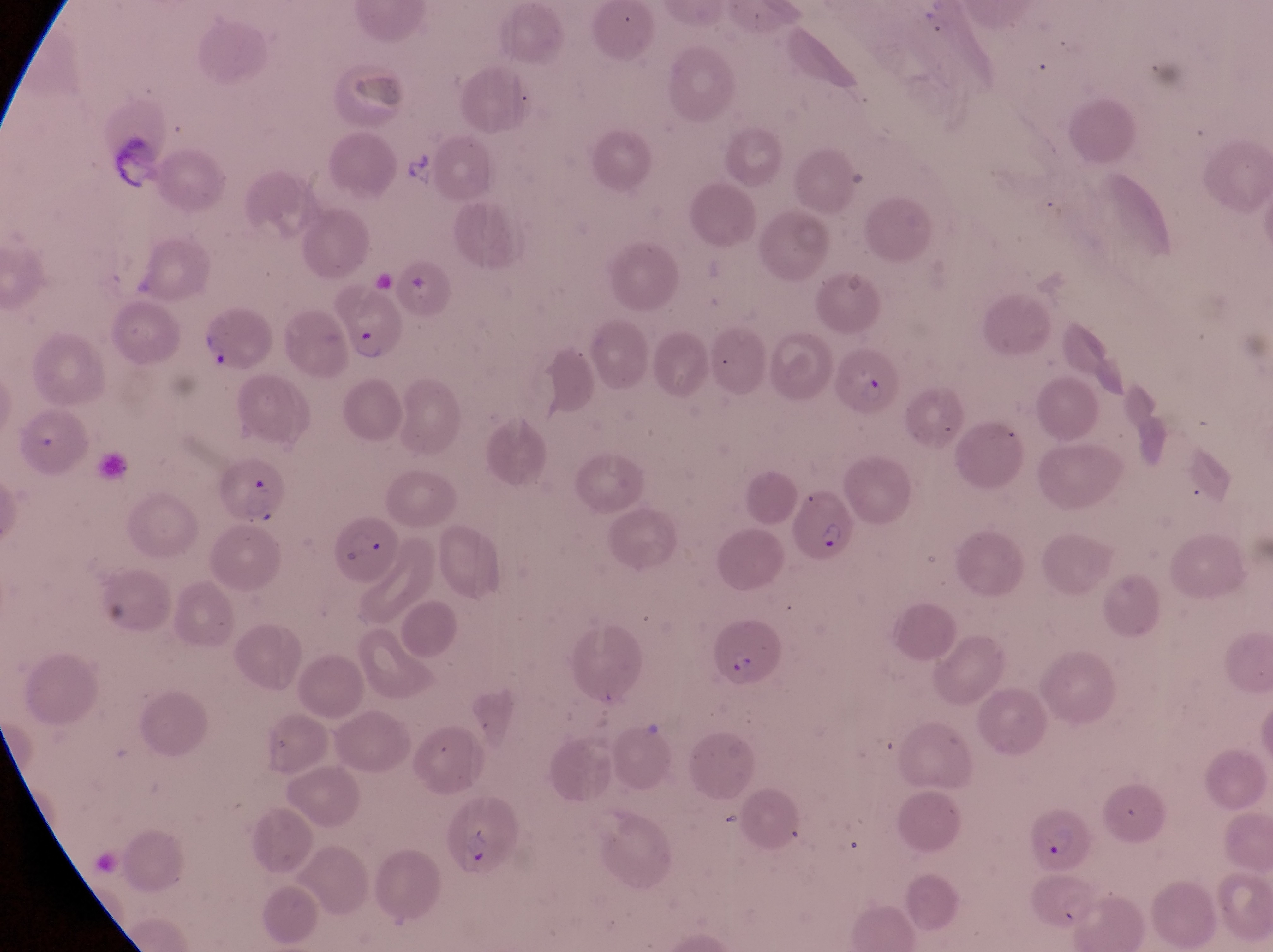

Approximate bounding boxes as {left, top, right, bottom} in pixels.
Summary:
  - Parasitised red blood cell locations: {339, 290, 402, 364}, {836, 348, 903, 423}, {13, 407, 90, 477}, {212, 457, 290, 527}, {787, 491, 861, 563}, {332, 519, 399, 586}, {711, 619, 788, 696}, {440, 802, 522, 880}, {1025, 811, 1099, 878}
  - Artifact (platelet-like body, stain precipitate, or debris) locations: {195, 312, 228, 365}
  - Preparation: thin blood film
  - Field of view: single
  - Image size: 1273×952 pixels
  - Capture: smartphone photograph through the eyepiece of an Olympus CX-23 microscope
  - Magnification: 1000x
  - Country: Uganda